Rate the background quality.
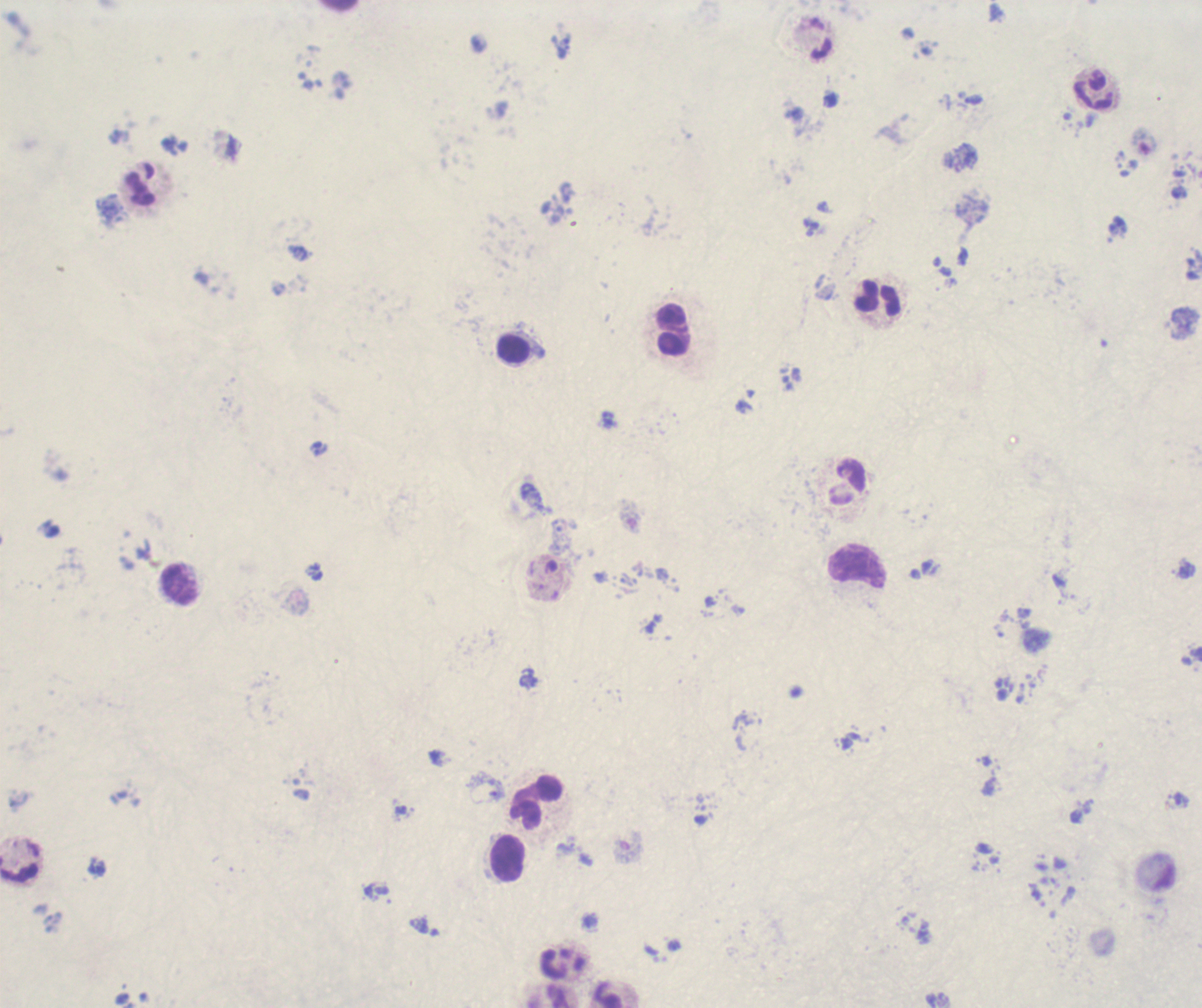

Poor.

Approximate centers as [x, y] in pixels.
Summary:
  - Trophozoite locations: [1181, 800]
  - Leukocyte locations: [1094, 92], [139, 190], [878, 298], [672, 330], [513, 347], [846, 483], [858, 566], [180, 584], [537, 802], [507, 859]
  - Preparation: thick blood smear
  - Field of view: one from this slide
  - Stain: Romanowsky
  - Image size: 1202×1008 pixels
  - Context: previously used in a real diagnosis
  - Magnification: 100x
  - Result: positive for malaria parasites